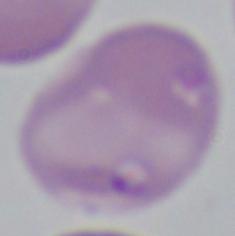

identification: Babesia
modality: photomicrograph
magnification: 1000x